Identify the parasite.
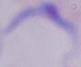
A trypanosome.

modality = photomicrograph
magnification = 1000x